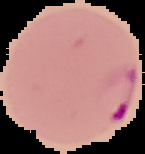
Image is 145×154 pixels. Segmented cell region on a black background. Result: malaria parasites detected. From a thin blood film.